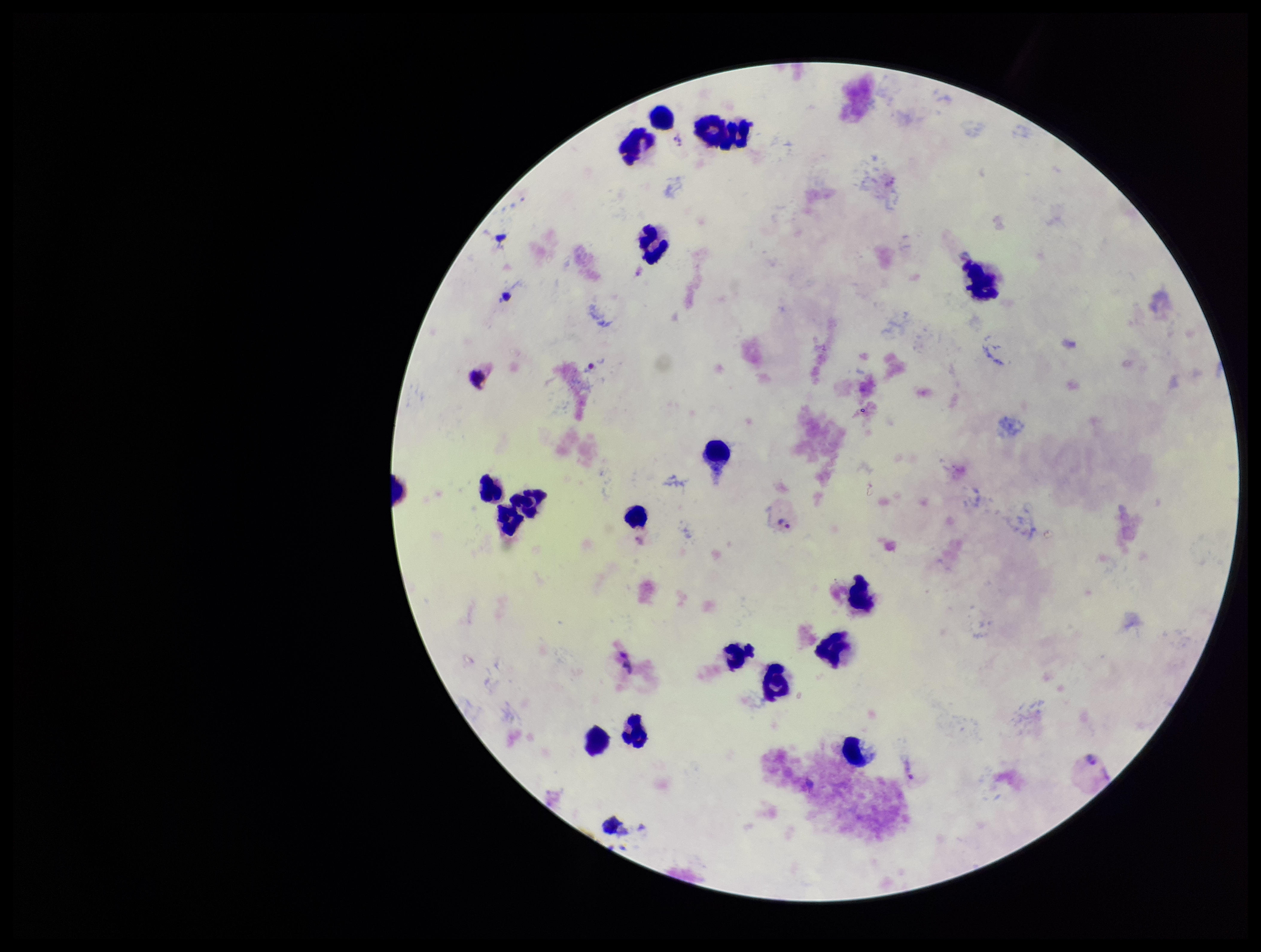

Summary:
  - Image size: 1261×952 pixels
  - Species reported for this patient: Plasmodium vivax
  - Capture: smartphone photograph through the microscope eyepiece
  - Preparation: thick
  - Patient malaria status: infected
  - Field of view: single
  - Parasite count: 5
  - Leukocyte count: 18
  - Stain: Giemsa
  - Plasmodium parasites: seen